Comment on the morphology of the red blood cells.
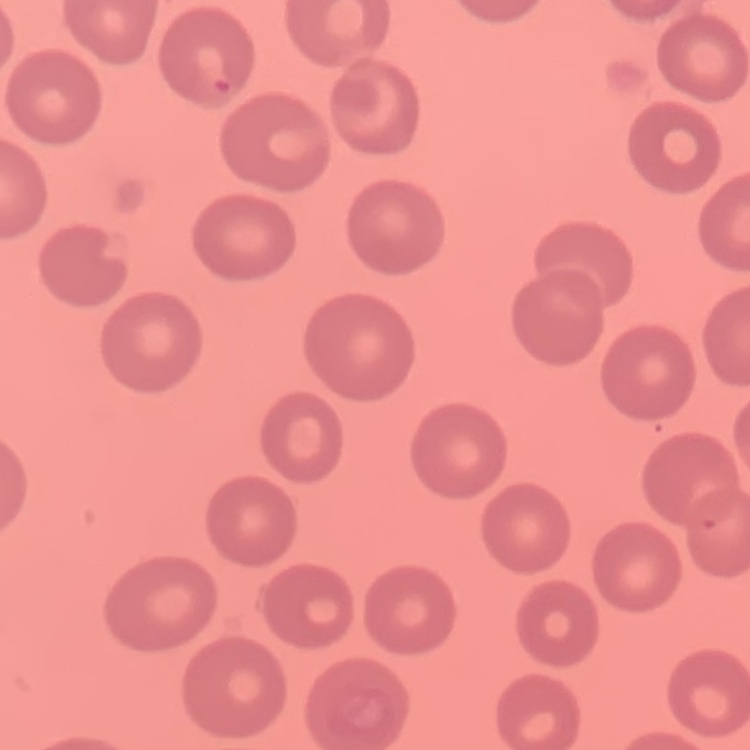

No rouleaux formation.

Summary:
  - Preparation: thin blood film
  - Image type: one tile cut from a larger photomicrograph
  - Stain: Field's or Giemsa